Name the parasite shown.
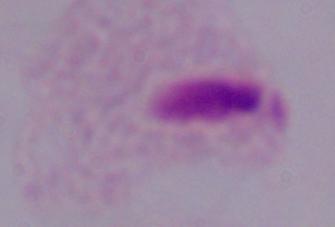
This is a trichomonad.

Summary:
  - Magnification: 1000x
  - Modality: micrograph